Locate and identify every blood parasite.
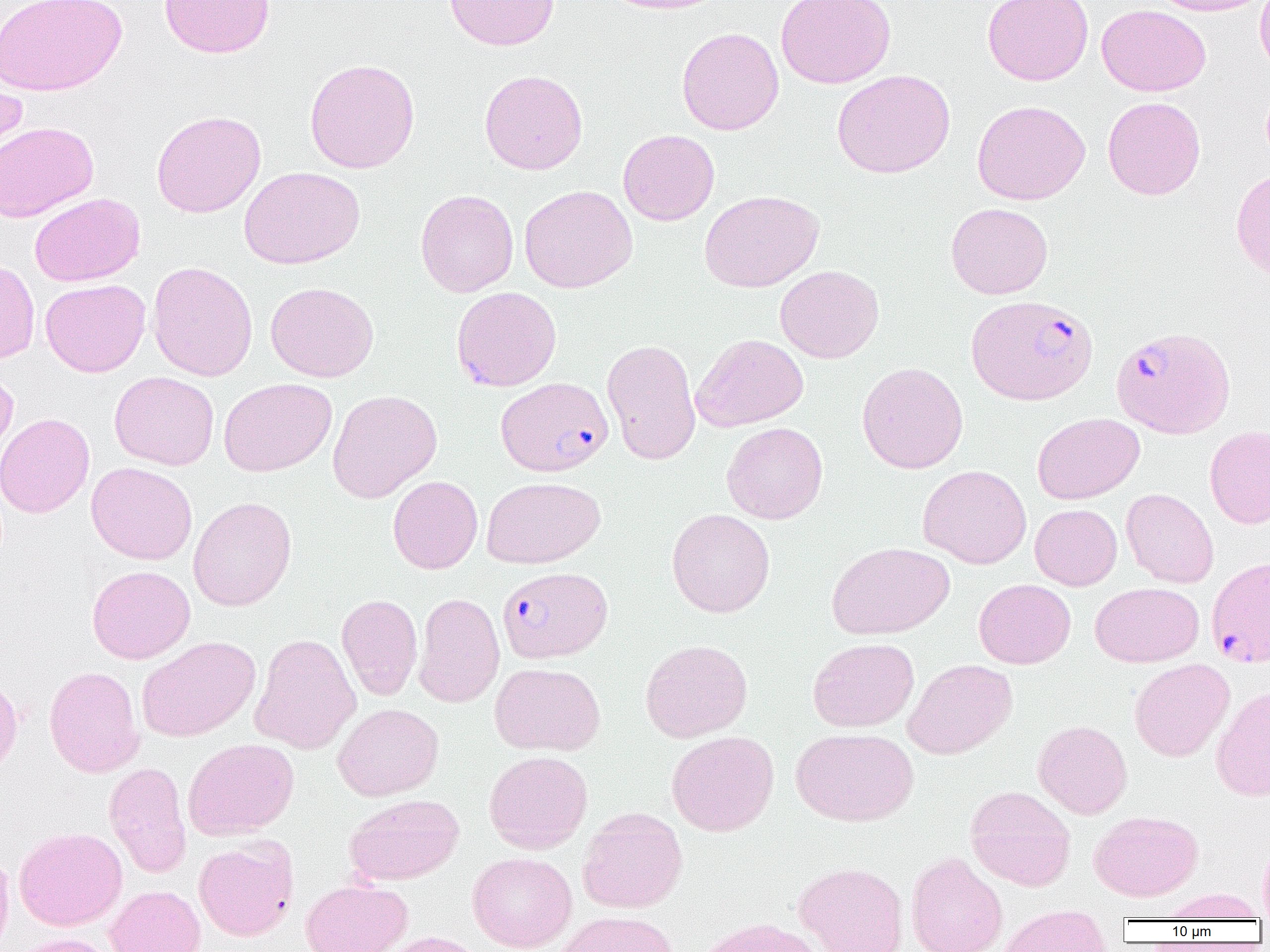

Approximate bounding boxes as (x1,y1)-(x2,y2) corner pairs in pixels.
Plasmodium falciparum-infected red blood cells: (451,286)-(561,391), (967,294)-(1098,405), (1111,326)-(1236,438), (496,377)-(613,477), (1207,556)-(1270,667), (497,566)-(612,663).
No Plasmodium ovale, Plasmodium malariae, Plasmodium vivax, Babesia divergens, or Trypanosoma brucei observed.

Summary:
  - Uninfected red blood cell locations: (0,0)-(127,97), (159,0)-(275,58), (444,0)-(560,51), (598,0)-(731,14), (776,0)-(896,89), (982,0)-(1093,85), (1147,0)-(1270,16), (1255,0)-(1270,79), (1097,4)-(1211,96), (676,26)-(784,135), (304,58)-(420,173), (479,69)-(588,175), (832,69)-(955,178), (0,71)-(27,172), (1102,96)-(1205,200), (971,100)-(1090,205), (151,110)-(266,218), (0,120)-(98,222), (618,129)-(720,225), (240,167)-(365,270), (1231,168)-(1270,281), (519,185)-(637,293), (415,189)-(519,297), (699,190)-(824,292), (29,193)-(145,286), (946,202)-(1053,300), (0,259)-(40,365), (147,261)-(258,381), (775,265)-(884,363), (40,279)-(150,377), (265,282)-(378,382), (691,333)-(809,431), (601,338)-(701,465), (857,362)-(968,473), (0,364)-(19,466), (109,371)-(219,470), (219,378)-(336,477), (327,389)-(442,502), (0,412)-(95,518), (1032,413)-(1144,504), (721,422)-(828,524), (1205,426)-(1270,529), (86,462)-(198,565), (917,464)-(1032,569), (388,476)-(483,574), (481,476)-(605,568), (1121,488)-(1219,588), (188,496)-(297,611), (1030,504)-(1122,590), (667,508)-(775,618), (826,541)-(954,640), (87,565)-(195,664), (974,579)-(1075,668), (1090,582)-(1203,667), (414,592)-(505,708), (337,593)-(423,700), (250,633)-(360,755), (137,636)-(260,742), (808,638)-(919,732), (639,639)-(753,742), (903,658)-(1017,759), (1129,658)-(1234,762), (490,662)-(605,755), (44,665)-(145,777), (0,672)-(23,778), (1211,684)-(1270,801), (332,703)-(444,800), (1033,719)-(1133,819), (790,727)-(918,826), (666,730)-(779,836), (182,738)-(299,840), (484,750)-(593,853), (104,762)-(192,878), (965,785)-(1076,891), (345,793)-(464,885), (577,807)-(688,913), (1089,810)-(1203,901), (14,827)-(127,931), (194,836)-(298,941), (1258,838)-(1270,922), (0,846)-(14,952), (467,851)-(577,952), (906,851)-(1007,952), (794,861)-(908,952), (301,879)-(412,952), (105,885)-(205,952), (1163,888)-(1264,921), (998,906)-(1110,952), (553,911)-(681,952), (693,917)-(825,952), (378,931)-(487,952), (10,933)-(118,952)
  - Slide-level diagnosis: Plasmodium falciparum
  - Modality: optical microscopy
  - Image size: 1270×952 pixels
  - Magnification: 1000x
  - Field of view: single
  - Preparation: thin blood smear